Report the malaria status of this cell.
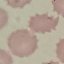

Uninfected.

Automatically extracted cell patch, resized to 64 × 64 pixels. Acquired by smartphone through the microscope eyepiece. Giemsa stain. Thin blood film.